Locate every Plasmodium falciparum-infected red blood cell.
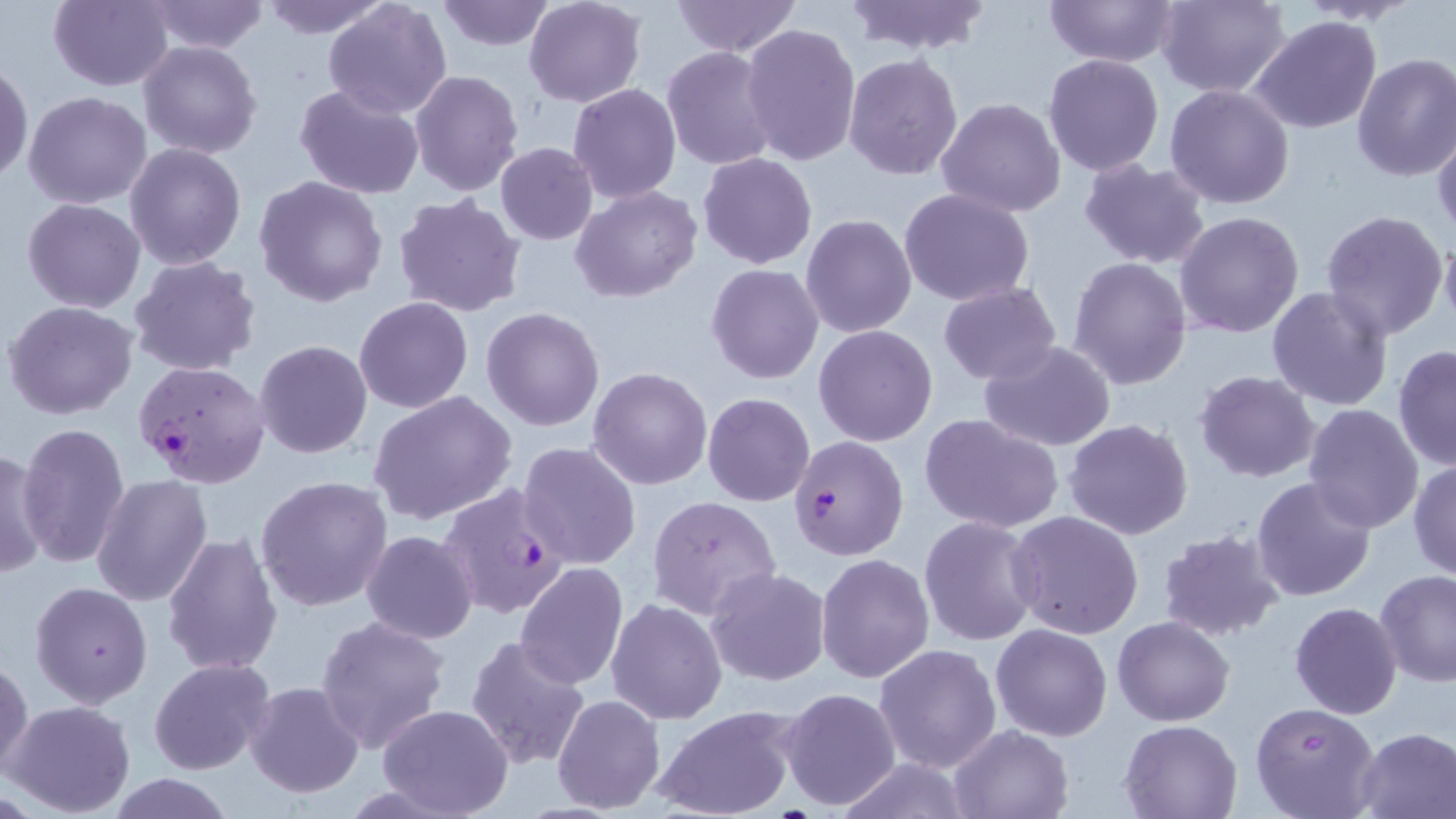
Approximate bounding boxes as (x1, y1, x2, y2) in pixels.
Plasmodium falciparum-infected red blood cells: (136, 360, 271, 488), (789, 435, 907, 560), (438, 484, 569, 618).

Summary:
  - Uninfected red blood cell locations: (47, 0, 176, 91), (148, 0, 270, 54), (260, 0, 393, 38), (669, 0, 802, 57), (839, 0, 996, 54), (1041, 0, 1181, 67), (1156, 0, 1291, 99), (322, 1, 452, 120), (433, 1, 557, 52), (524, 1, 646, 108), (1248, 16, 1384, 135), (740, 24, 861, 167), (138, 40, 263, 160), (662, 46, 779, 171), (844, 53, 964, 179), (1042, 53, 1164, 176), (1352, 53, 1456, 181), (0, 58, 33, 187), (410, 69, 524, 195), (568, 83, 682, 204), (1165, 84, 1296, 209), (294, 85, 425, 200), (24, 91, 152, 210), (936, 97, 1066, 218), (1432, 124, 1456, 241), (125, 142, 247, 269), (496, 143, 597, 245), (698, 153, 819, 270), (1079, 159, 1212, 270), (254, 174, 389, 307), (572, 185, 702, 303), (898, 188, 1037, 308), (393, 195, 527, 318), (21, 197, 147, 313), (1319, 209, 1452, 342), (1174, 211, 1304, 338), (800, 213, 918, 339), (1439, 231, 1456, 336), (129, 255, 260, 376), (1068, 257, 1193, 392), (706, 263, 824, 384), (937, 284, 1063, 385), (1267, 285, 1395, 413), (353, 297, 474, 413), (4, 300, 140, 421), (480, 307, 605, 432), (814, 324, 938, 447), (254, 339, 374, 459), (977, 341, 1117, 452), (1392, 344, 1455, 471), (587, 366, 713, 490), (1195, 370, 1321, 483), (367, 391, 518, 526), (703, 393, 815, 507), (1301, 403, 1424, 535), (919, 412, 1064, 534), (1063, 418, 1194, 540), (15, 422, 131, 567), (517, 441, 642, 569), (0, 446, 51, 581), (1409, 458, 1456, 581), (92, 475, 213, 608), (255, 475, 393, 614), (1251, 477, 1377, 602), (648, 495, 781, 619), (1009, 511, 1144, 639), (920, 515, 1042, 647), (1157, 527, 1287, 641), (362, 530, 478, 643), (161, 531, 284, 676), (816, 552, 935, 685), (515, 563, 629, 688), (706, 567, 831, 686), (1375, 570, 1456, 687), (839, 576, 968, 750), (30, 581, 153, 709), (605, 598, 728, 723), (1288, 603, 1402, 719), (317, 614, 451, 752), (1112, 614, 1234, 726), (990, 623, 1113, 741), (466, 635, 592, 770), (874, 643, 1001, 774), (1, 653, 32, 783), (149, 657, 276, 776), (243, 680, 365, 800), (779, 686, 902, 812), (552, 693, 666, 813), (5, 699, 136, 817), (1250, 701, 1383, 819), (375, 703, 514, 818), (649, 705, 801, 819), (1120, 719, 1241, 818), (947, 724, 1075, 817), (1352, 727, 1456, 817), (829, 757, 978, 818), (109, 775, 234, 818)
  - Slide-level diagnosis: Plasmodium falciparum
  - Field of view: single
  - Preparation: thin blood smear
  - Image size: 1456×819 pixels
  - Modality: optical microscopy
  - Magnification: 1000x
  - Stain: May-Grünwald-Giemsa